Name the parasite shown.
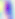

This is Toxoplasma gondii.

Summary:
  - Modality: micrograph
  - Magnification: 400x